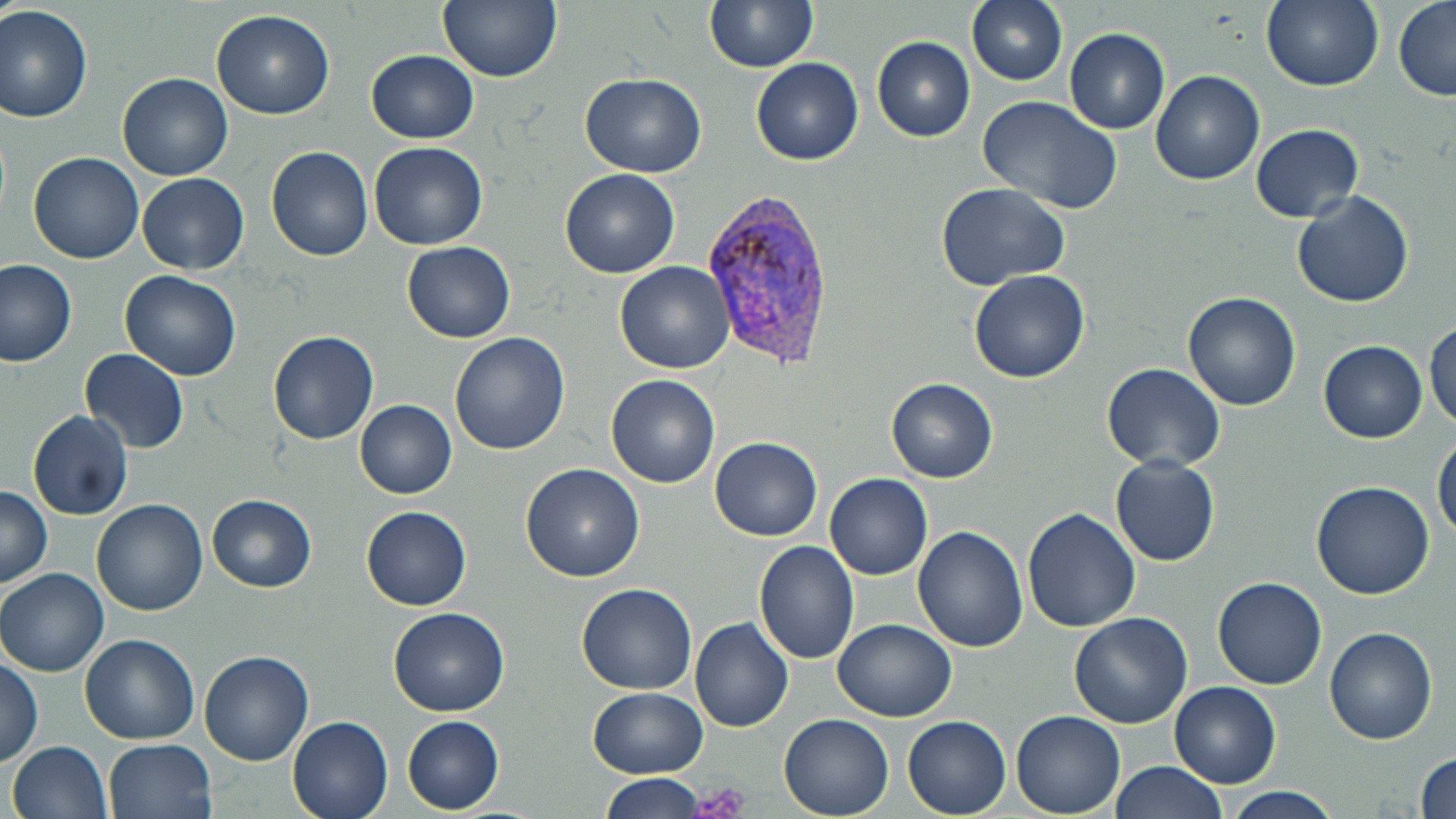
Approximate bounding boxes as named x1/y1/x2/y2 corners in pixels. Platelet locations: (x1=690, y1=782, x2=752, y2=819). Plasmodium vivax-infected red blood cell locations: (x1=701, y1=191, x2=835, y2=366). Uninfected red blood cell locations: (x1=439, y1=0, x2=562, y2=83), (x1=705, y1=0, x2=817, y2=73), (x1=967, y1=0, x2=1068, y2=85), (x1=1260, y1=0, x2=1383, y2=91), (x1=1391, y1=0, x2=1455, y2=102), (x1=0, y1=4, x2=96, y2=124), (x1=212, y1=9, x2=335, y2=119), (x1=1064, y1=28, x2=1170, y2=134), (x1=872, y1=36, x2=975, y2=141), (x1=368, y1=49, x2=479, y2=143), (x1=752, y1=57, x2=863, y2=165), (x1=1151, y1=70, x2=1264, y2=185), (x1=119, y1=72, x2=233, y2=180), (x1=581, y1=72, x2=707, y2=177), (x1=975, y1=95, x2=1122, y2=216), (x1=1251, y1=124, x2=1362, y2=221), (x1=369, y1=142, x2=488, y2=251), (x1=266, y1=145, x2=374, y2=261), (x1=29, y1=151, x2=144, y2=262), (x1=559, y1=168, x2=680, y2=277), (x1=136, y1=173, x2=249, y2=274), (x1=935, y1=182, x2=1072, y2=291), (x1=1292, y1=190, x2=1414, y2=309), (x1=403, y1=241, x2=516, y2=342), (x1=0, y1=259, x2=78, y2=367), (x1=615, y1=261, x2=734, y2=374), (x1=121, y1=270, x2=242, y2=383), (x1=970, y1=270, x2=1090, y2=382), (x1=1183, y1=292, x2=1302, y2=409), (x1=1427, y1=322, x2=1455, y2=433), (x1=268, y1=330, x2=379, y2=444), (x1=450, y1=331, x2=572, y2=455), (x1=1319, y1=341, x2=1427, y2=442), (x1=81, y1=349, x2=189, y2=453), (x1=1101, y1=363, x2=1225, y2=474), (x1=607, y1=375, x2=720, y2=489), (x1=887, y1=378, x2=998, y2=483), (x1=355, y1=401, x2=457, y2=499), (x1=28, y1=410, x2=133, y2=520), (x1=710, y1=436, x2=822, y2=541), (x1=1434, y1=437, x2=1455, y2=543), (x1=1111, y1=455, x2=1220, y2=566), (x1=520, y1=463, x2=644, y2=581), (x1=824, y1=474, x2=932, y2=579), (x1=1311, y1=481, x2=1436, y2=601), (x1=0, y1=484, x2=53, y2=590), (x1=206, y1=494, x2=317, y2=592), (x1=92, y1=498, x2=207, y2=615), (x1=361, y1=506, x2=471, y2=610), (x1=1023, y1=507, x2=1140, y2=632), (x1=913, y1=526, x2=1028, y2=651), (x1=754, y1=540, x2=861, y2=664), (x1=1, y1=568, x2=109, y2=677), (x1=1213, y1=576, x2=1327, y2=689), (x1=577, y1=583, x2=696, y2=694), (x1=387, y1=606, x2=510, y2=716), (x1=1069, y1=611, x2=1192, y2=728), (x1=690, y1=618, x2=794, y2=733), (x1=834, y1=618, x2=955, y2=721), (x1=1324, y1=627, x2=1439, y2=744), (x1=80, y1=634, x2=200, y2=745), (x1=200, y1=649, x2=313, y2=767), (x1=1, y1=651, x2=43, y2=768), (x1=1169, y1=682, x2=1282, y2=788), (x1=589, y1=687, x2=707, y2=777), (x1=1011, y1=710, x2=1125, y2=816), (x1=780, y1=713, x2=893, y2=818), (x1=286, y1=715, x2=393, y2=819), (x1=401, y1=715, x2=505, y2=813), (x1=902, y1=715, x2=1012, y2=817), (x1=104, y1=738, x2=217, y2=819), (x1=8, y1=740, x2=114, y2=819), (x1=1414, y1=751, x2=1455, y2=818), (x1=1108, y1=760, x2=1230, y2=819), (x1=599, y1=774, x2=705, y2=818), (x1=1224, y1=787, x2=1345, y2=817). Slide-level diagnosis: Plasmodium vivax. One field of a larger specimen. Optical microscopy. Image is 1456×819 pixels. Thin blood film. Captured at 1000x magnification. May-Grünwald-Giemsa stain.